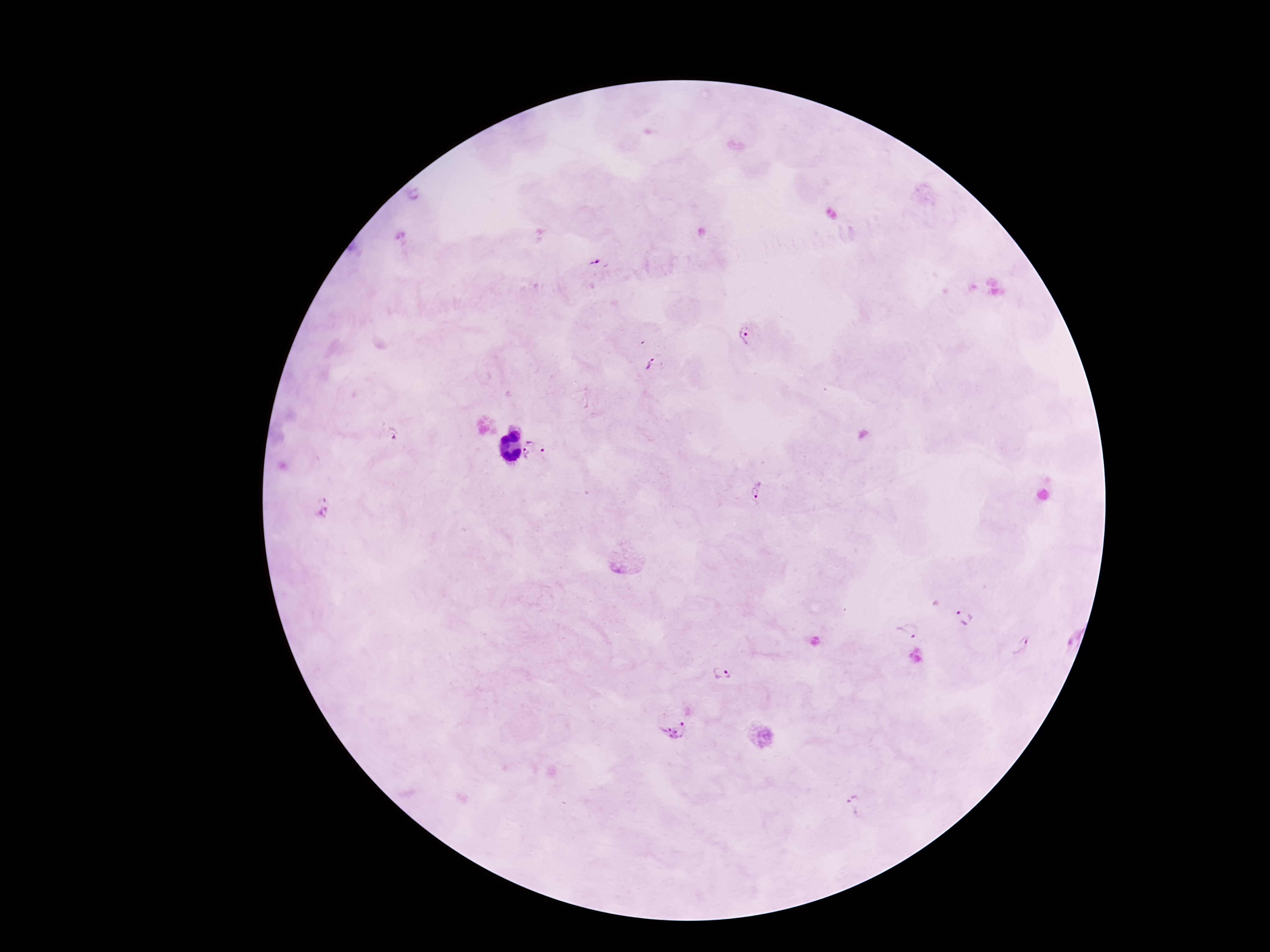
Approximate centers as [x, y] in pixels.
Summary:
  - Plasmodium parasite locations: [597, 263], [748, 335], [649, 365], [540, 436], [527, 456], [758, 492], [323, 508], [962, 619], [907, 631], [1026, 645], [724, 676], [675, 730], [859, 807]
  - Preparation: thick peripheral-blood smear
  - Image size: 1270×952 pixels
  - Stain: Giemsa
  - Capture: smartphone camera through the microscope eyepiece
  - Field of view: single
  - Magnification: 100x
  - Patient malaria status: infected